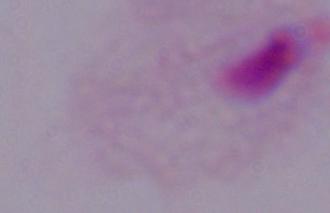

modality = micrograph
magnification = 1000x
identification = trichomonad